Give the position of every Plasmodium parasite.
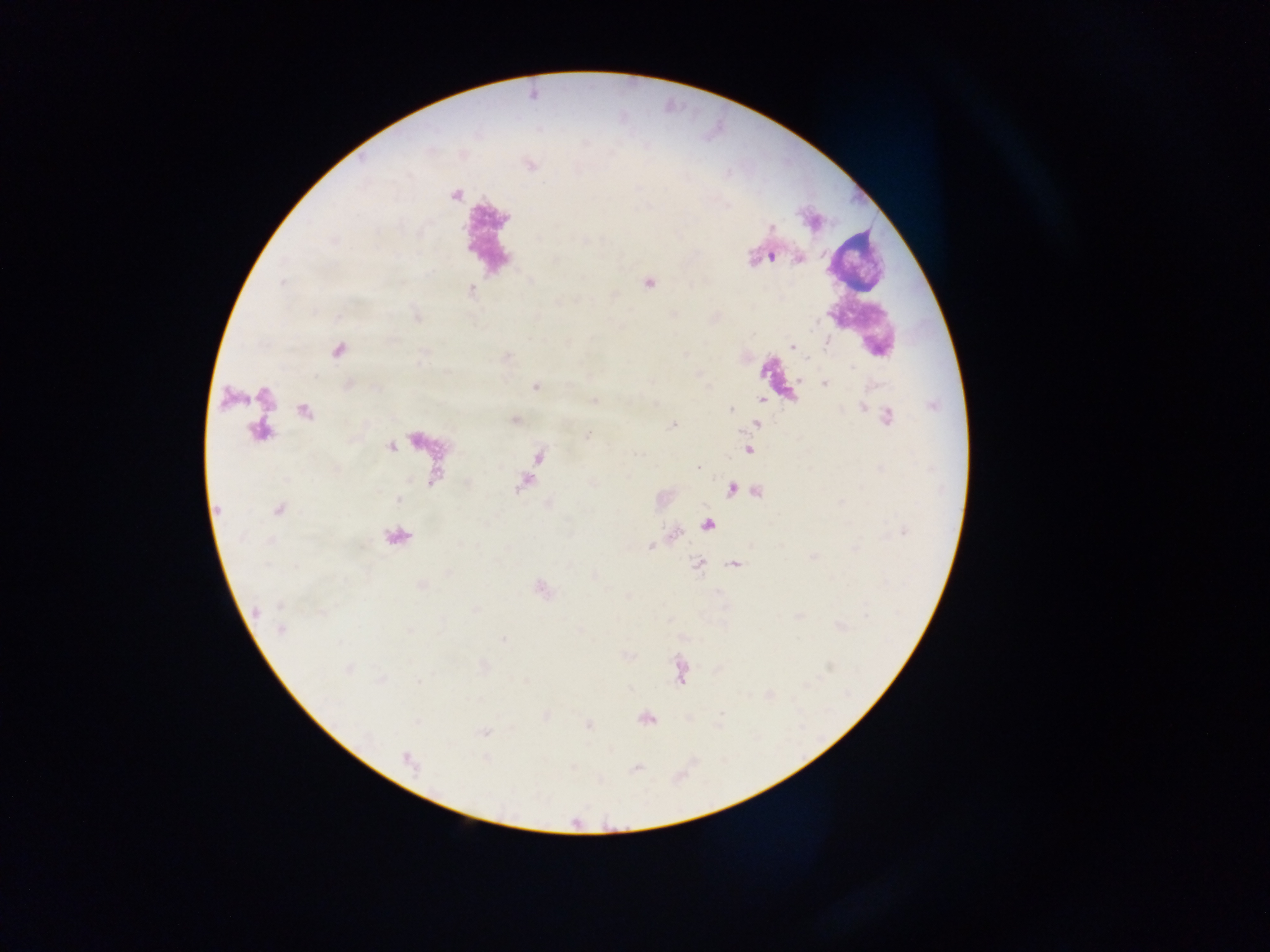

Approximate centers as x y in pixels.
Plasmodium parasites: 773 257; 827 344; 792 346; 809 358; 851 367; 824 384; 535 387; 731 409; 888 416; 673 426; 588 436; 698 468; 650 547; 282 630; 348 670.

Leukocyte locations: 856 261. Collected in Ghana. Image is 1270×952 pixels. Mobile-phone photograph taken through the microscope. Thick blood film. Single field of view.